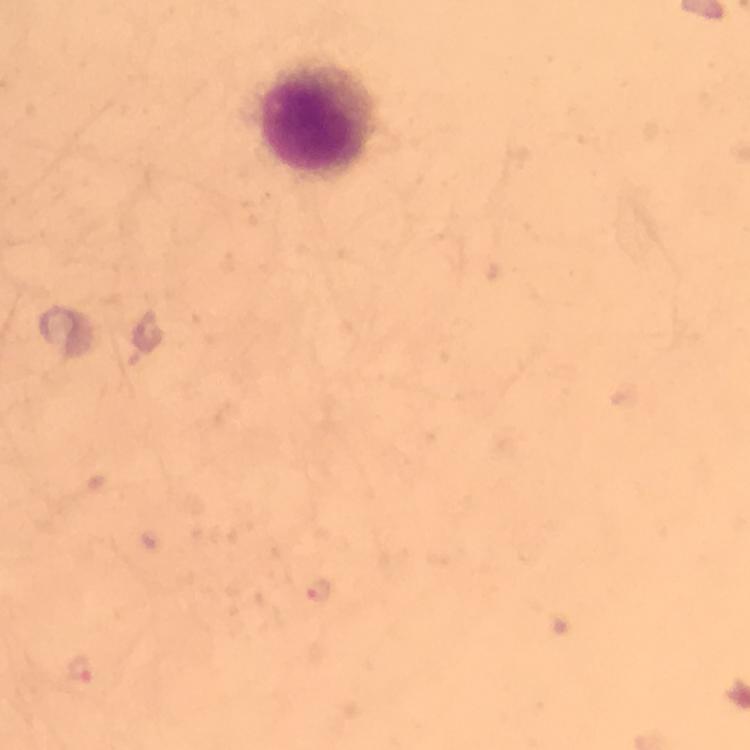 Approximate centers as {x, y} in pixels. Malaria parasite locations: {80, 669}. Leukocyte locations: {317, 120}. 100x magnification. From a diagnostic examination for malaria. Image is 750×750 pixels. Cropped region of a single field of view. Photographed with a smartphone mounted on the microscope. Giemsa stain. Immersion oil applied. Thick smear.